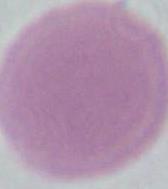 Photomicrograph. Captured at 1000x magnification. An erythrocyte is seen.